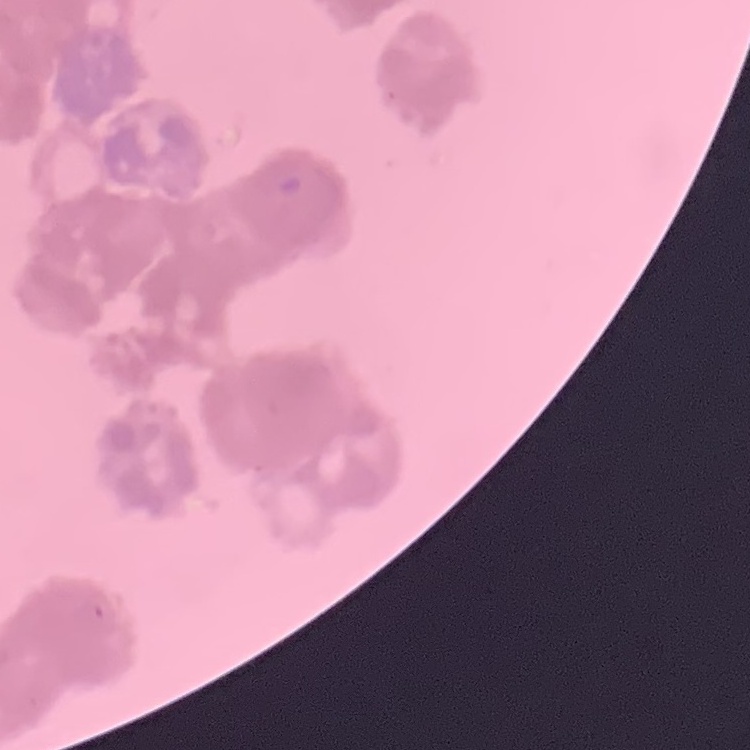
Summary:
  - Erythrocyte morphology: rouleaux formation
  - Image type: square crop of a larger photomicrograph
  - Preparation: thin blood film
  - Stain: Field's or Giemsa